Report the malaria status of this cell.
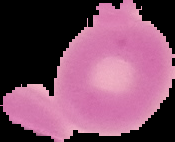
It is uninfected.

Image is 175×142 pixels. Segmented cell region on a black background. From a thin blood film.